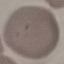

malaria status = uninfected
preparation = thin blood film
stain = Giemsa
capture = smartphone through the microscope eyepiece
image type = automatically extracted cell patch, resized to 64 × 64 pixels